Give the extent of all Plasmodium ovale-infected red blood cells.
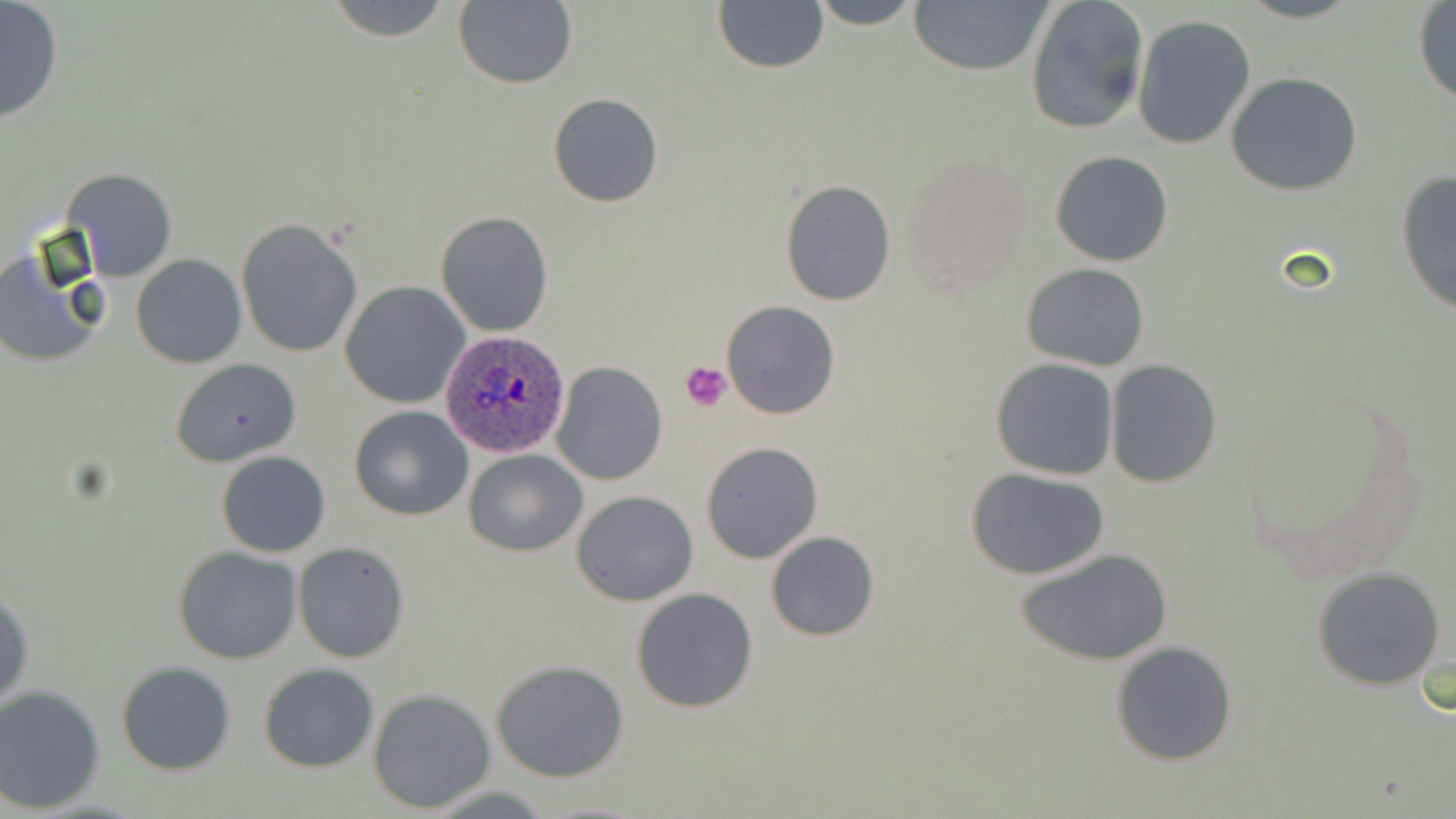

Approximate bounding boxes as named x1/y1/x2/y2 corners in pixels.
Plasmodium ovale-infected red blood cells: (x1=442, y1=331, x2=571, y2=459).

slide-level diagnosis = Plasmodium ovale
image size = 1456×819 pixels
uninfected red blood cell locations = approximate bounding boxes as named x1/y1/x2/y2 corners in pixels: (x1=325, y1=0, x2=453, y2=41), (x1=713, y1=0, x2=828, y2=74), (x1=810, y1=0, x2=923, y2=28), (x1=906, y1=0, x2=1053, y2=75), (x1=1023, y1=0, x2=1150, y2=136), (x1=0, y1=1, x2=65, y2=126), (x1=453, y1=1, x2=577, y2=88), (x1=1413, y1=3, x2=1456, y2=105), (x1=1133, y1=15, x2=1257, y2=151), (x1=1227, y1=71, x2=1362, y2=196), (x1=548, y1=93, x2=663, y2=208), (x1=1051, y1=150, x2=1174, y2=268), (x1=900, y1=152, x2=1033, y2=289), (x1=61, y1=168, x2=177, y2=279), (x1=1396, y1=169, x2=1455, y2=316), (x1=779, y1=178, x2=897, y2=305), (x1=435, y1=210, x2=555, y2=337), (x1=235, y1=218, x2=363, y2=359), (x1=0, y1=248, x2=107, y2=369), (x1=132, y1=254, x2=246, y2=369), (x1=1021, y1=263, x2=1150, y2=369), (x1=340, y1=282, x2=469, y2=409), (x1=722, y1=300, x2=839, y2=419), (x1=990, y1=358, x2=1120, y2=481), (x1=1104, y1=359, x2=1221, y2=487), (x1=171, y1=360, x2=300, y2=467), (x1=551, y1=361, x2=668, y2=485), (x1=349, y1=406, x2=473, y2=520), (x1=700, y1=442, x2=822, y2=565), (x1=465, y1=449, x2=587, y2=557), (x1=216, y1=451, x2=332, y2=557), (x1=968, y1=467, x2=1110, y2=580), (x1=573, y1=491, x2=697, y2=606), (x1=765, y1=531, x2=880, y2=641), (x1=292, y1=542, x2=410, y2=663), (x1=173, y1=546, x2=303, y2=664), (x1=1018, y1=546, x2=1174, y2=665), (x1=1311, y1=566, x2=1447, y2=690), (x1=1, y1=587, x2=35, y2=714), (x1=631, y1=587, x2=759, y2=714), (x1=1111, y1=640, x2=1239, y2=766), (x1=491, y1=659, x2=630, y2=782), (x1=116, y1=660, x2=237, y2=774), (x1=258, y1=663, x2=379, y2=771), (x1=0, y1=685, x2=106, y2=812), (x1=367, y1=688, x2=497, y2=813)
modality = optical microscopy
stain = May-Grünwald-Giemsa
field of view = one of a larger specimen
preparation = thin blood film
magnification = 1000x
platelet locations = approximate bounding boxes as named x1/y1/x2/y2 corners in pixels: (x1=679, y1=361, x2=734, y2=410)